Assess the morphology of the erythrocytes.
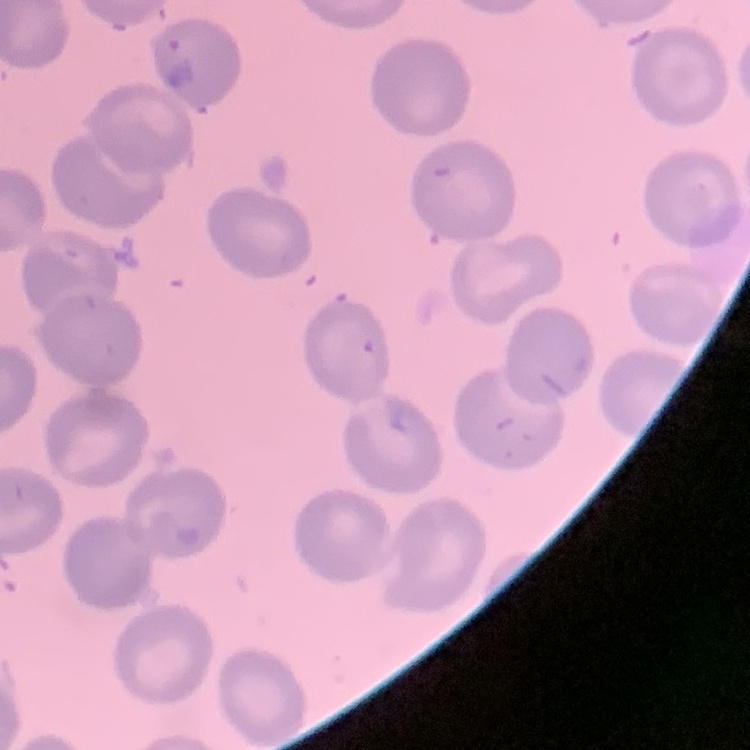
No rouleaux formation.

preparation = thin blood film
image type = square crop of a larger photomicrograph
stain = Field's or Giemsa